Assess this cell for malaria.
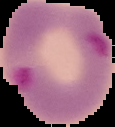
It is parasitized.

{
  "preparation": "thin blood film",
  "image_type": "segmented cell region on a black background",
  "image_size": "115×127 pixels"
}